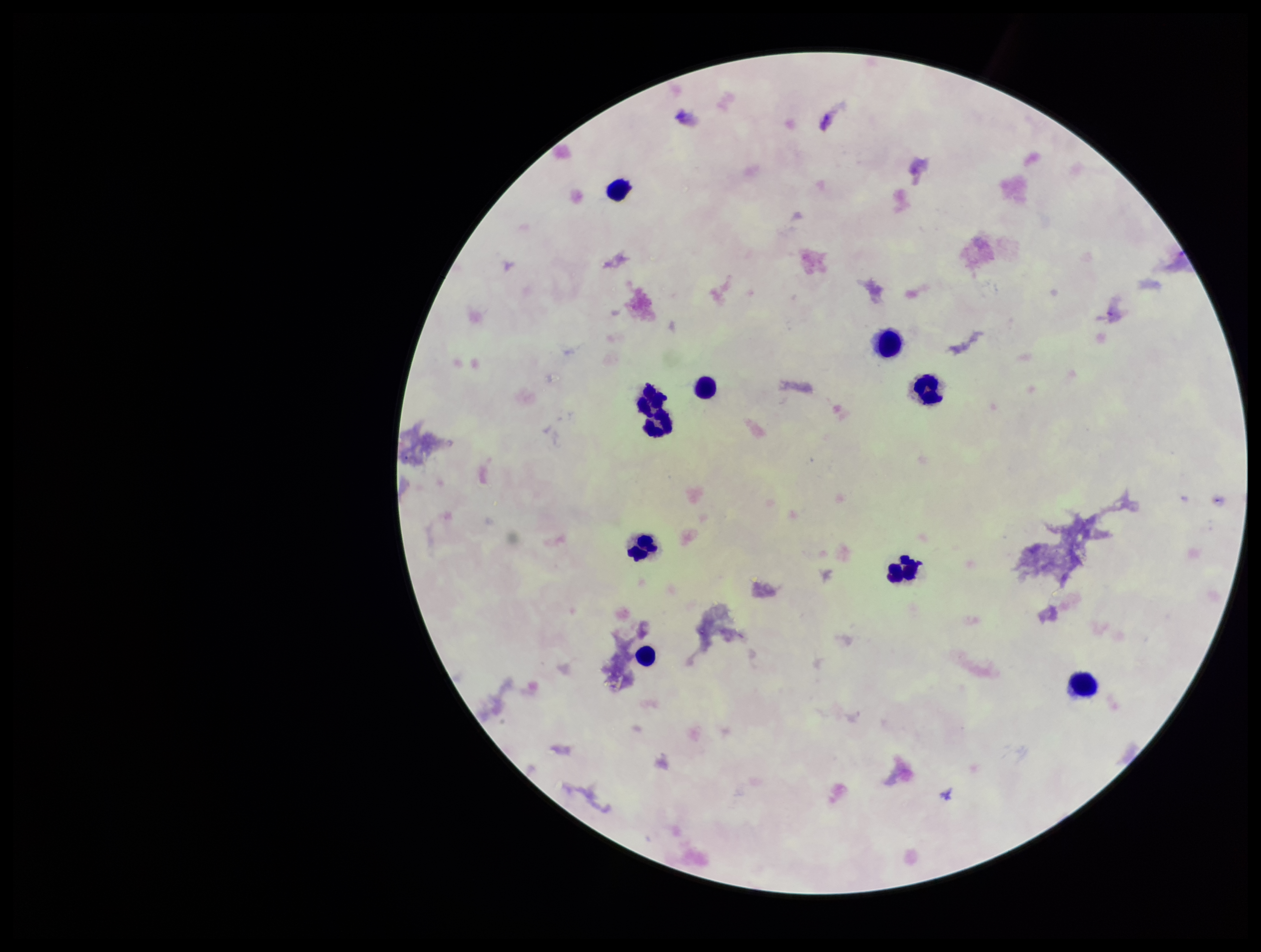
Summary:
  - Preparation: thick smear
  - Leukocyte count: 9
  - Stain: Giemsa
  - Parasite count: 0
  - Capture: smartphone photograph through the microscope eyepiece
  - Image size: 1261×952 pixels
  - Plasmodium parasites: none identified
  - Patient malaria status: negative
  - Field of view: one from this slide